Name the cell type shown.
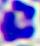

A leukocyte.

Summary:
  - Modality: photomicrograph
  - Magnification: 400x